Assess this cell for malaria.
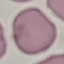
Uninfected.

Cell patch, automatically extracted from a larger field of view and resized to 64 × 64 pixels. Photographed with a smartphone camera at the microscope eyepiece. Giemsa stain. Thin blood film.